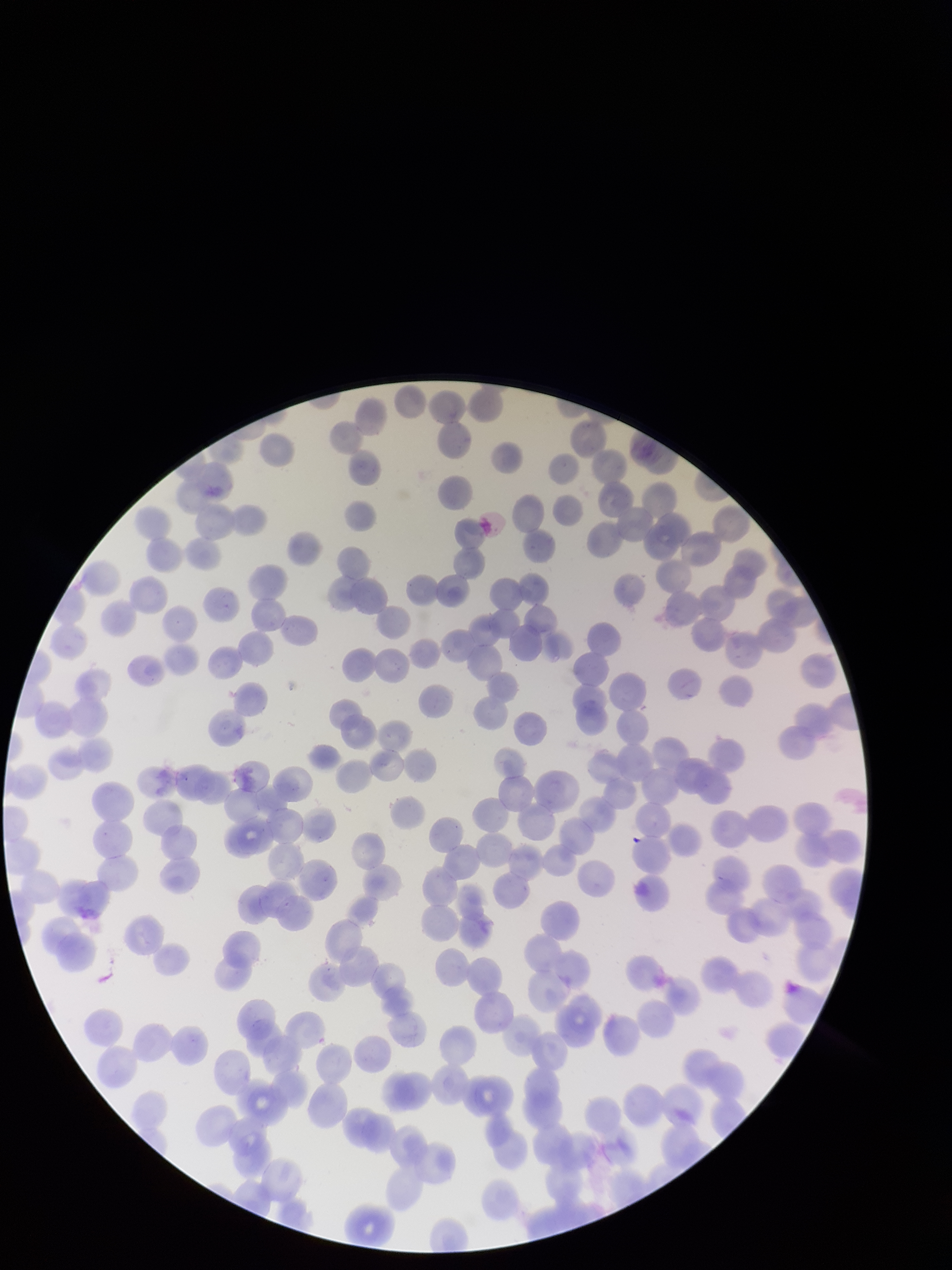 Preparation: thin. One field from this slide. Patient malaria status: infected. Giemsa stain. Parasitized red blood cells: none seen. Red blood cell count: 229. Photographed through the microscope eyepiece with a smartphone camera. Species reported for this patient: Plasmodium falciparum. Image is 952×1270 pixels. Parasitized red blood cell count: 0.